Name the blood parasite species.
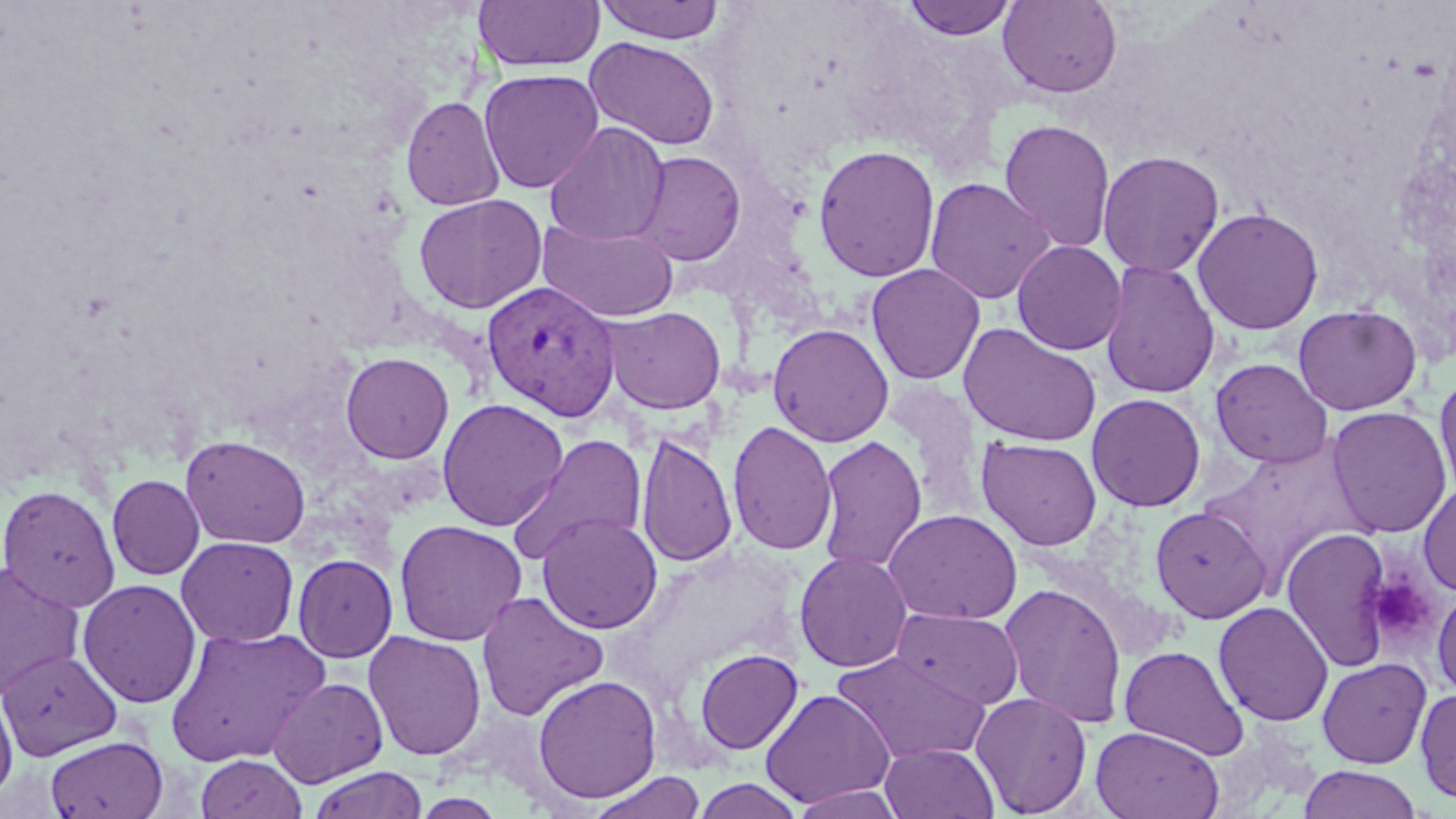

Plasmodium vivax.

Summary:
  - Coordinate format: approximate bounding boxes as named x1/y1/x2/y2 corners in pixels
  - Platelet locations: (x1=1367, y1=572, x2=1438, y2=647)
  - Uninfected red blood cell locations: (x1=473, y1=0, x2=605, y2=72), (x1=594, y1=0, x2=726, y2=44), (x1=901, y1=0, x2=1020, y2=40), (x1=998, y1=0, x2=1123, y2=99), (x1=585, y1=36, x2=721, y2=150), (x1=478, y1=69, x2=604, y2=194), (x1=401, y1=95, x2=505, y2=211), (x1=999, y1=118, x2=1116, y2=254), (x1=544, y1=122, x2=670, y2=248), (x1=812, y1=144, x2=941, y2=282), (x1=630, y1=150, x2=747, y2=266), (x1=1096, y1=150, x2=1225, y2=277), (x1=924, y1=177, x2=1055, y2=305), (x1=413, y1=193, x2=548, y2=314), (x1=1191, y1=206, x2=1324, y2=335), (x1=538, y1=218, x2=679, y2=323), (x1=1011, y1=240, x2=1127, y2=356), (x1=1100, y1=260, x2=1220, y2=399), (x1=865, y1=263, x2=985, y2=385), (x1=1293, y1=304, x2=1422, y2=416), (x1=602, y1=305, x2=727, y2=414), (x1=768, y1=323, x2=894, y2=447), (x1=958, y1=323, x2=1104, y2=447), (x1=340, y1=351, x2=454, y2=464), (x1=1210, y1=358, x2=1333, y2=468), (x1=1435, y1=367, x2=1456, y2=501), (x1=1086, y1=393, x2=1206, y2=512), (x1=437, y1=398, x2=569, y2=531), (x1=1325, y1=405, x2=1452, y2=539), (x1=728, y1=420, x2=837, y2=556), (x1=636, y1=432, x2=737, y2=568), (x1=507, y1=433, x2=649, y2=565), (x1=180, y1=434, x2=311, y2=549), (x1=815, y1=434, x2=927, y2=574), (x1=976, y1=437, x2=1103, y2=551), (x1=1198, y1=440, x2=1363, y2=584), (x1=107, y1=474, x2=204, y2=580), (x1=1416, y1=483, x2=1456, y2=596), (x1=0, y1=484, x2=121, y2=612), (x1=1150, y1=505, x2=1271, y2=624), (x1=884, y1=509, x2=1023, y2=625), (x1=536, y1=512, x2=663, y2=634), (x1=394, y1=519, x2=527, y2=646), (x1=1282, y1=526, x2=1394, y2=673), (x1=176, y1=535, x2=299, y2=647), (x1=794, y1=550, x2=913, y2=673), (x1=293, y1=553, x2=398, y2=662), (x1=0, y1=561, x2=86, y2=700), (x1=78, y1=578, x2=201, y2=708), (x1=998, y1=582, x2=1128, y2=728), (x1=1432, y1=586, x2=1456, y2=701), (x1=476, y1=591, x2=608, y2=722), (x1=1213, y1=600, x2=1334, y2=727), (x1=893, y1=607, x2=1024, y2=709), (x1=164, y1=626, x2=330, y2=767), (x1=363, y1=630, x2=487, y2=761), (x1=1119, y1=645, x2=1250, y2=759), (x1=0, y1=647, x2=123, y2=760), (x1=694, y1=648, x2=803, y2=755), (x1=833, y1=650, x2=991, y2=764), (x1=1317, y1=657, x2=1432, y2=769), (x1=532, y1=674, x2=662, y2=803), (x1=268, y1=676, x2=388, y2=787), (x1=0, y1=685, x2=18, y2=805), (x1=1415, y1=687, x2=1456, y2=806), (x1=760, y1=688, x2=895, y2=809), (x1=970, y1=692, x2=1092, y2=816), (x1=1091, y1=725, x2=1224, y2=819), (x1=45, y1=735, x2=168, y2=819), (x1=880, y1=742, x2=999, y2=819), (x1=196, y1=753, x2=306, y2=819), (x1=1298, y1=765, x2=1423, y2=819), (x1=307, y1=767, x2=429, y2=819), (x1=586, y1=771, x2=707, y2=819), (x1=692, y1=778, x2=804, y2=819), (x1=789, y1=785, x2=906, y2=818)
  - Plasmodium vivax-infected red blood cell locations: (x1=483, y1=280, x2=621, y2=420)
  - Field of view: single
  - Modality: light microscopy
  - Preparation: thin blood film
  - Image size: 1456×819 pixels
  - Stain: May-Grünwald-Giemsa
  - Magnification: 1000x